Comment on the morphology of the erythrocytes.
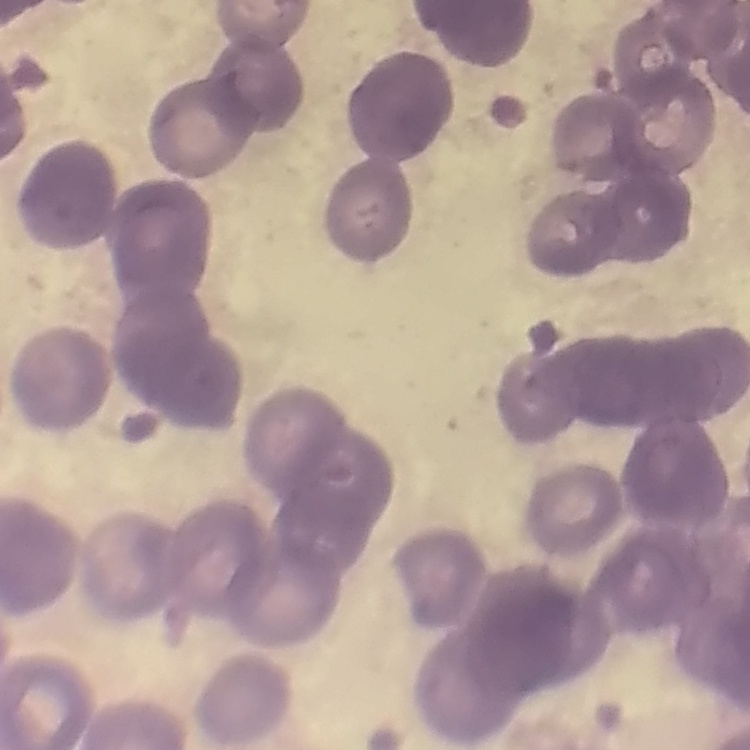
They show rouleaux formation.

One tile cut from a larger photomicrograph. Thin blood film. Field's or Giemsa stain.